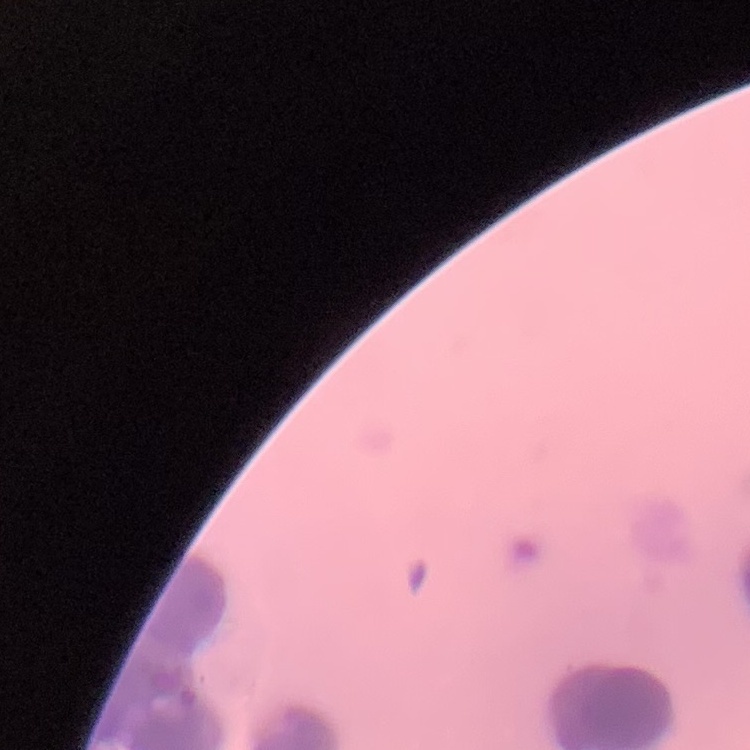 The erythrocytes exhibit rouleaux formation. Thin peripheral smear. Square crop of a larger photomicrograph. Stained with either Field's or Giemsa.